Assess this cell for malaria.
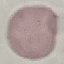

It is uninfected.

capture = smartphone through the microscope eyepiece
image type = cell patch, automatically extracted from a larger field of view and resized to 64 × 64 pixels
stain = Giemsa
preparation = thin smear